Identify the cell.
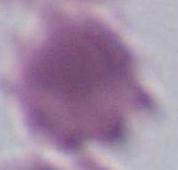

This is an erythrocyte.

Captured at 1000x magnification. Micrograph.